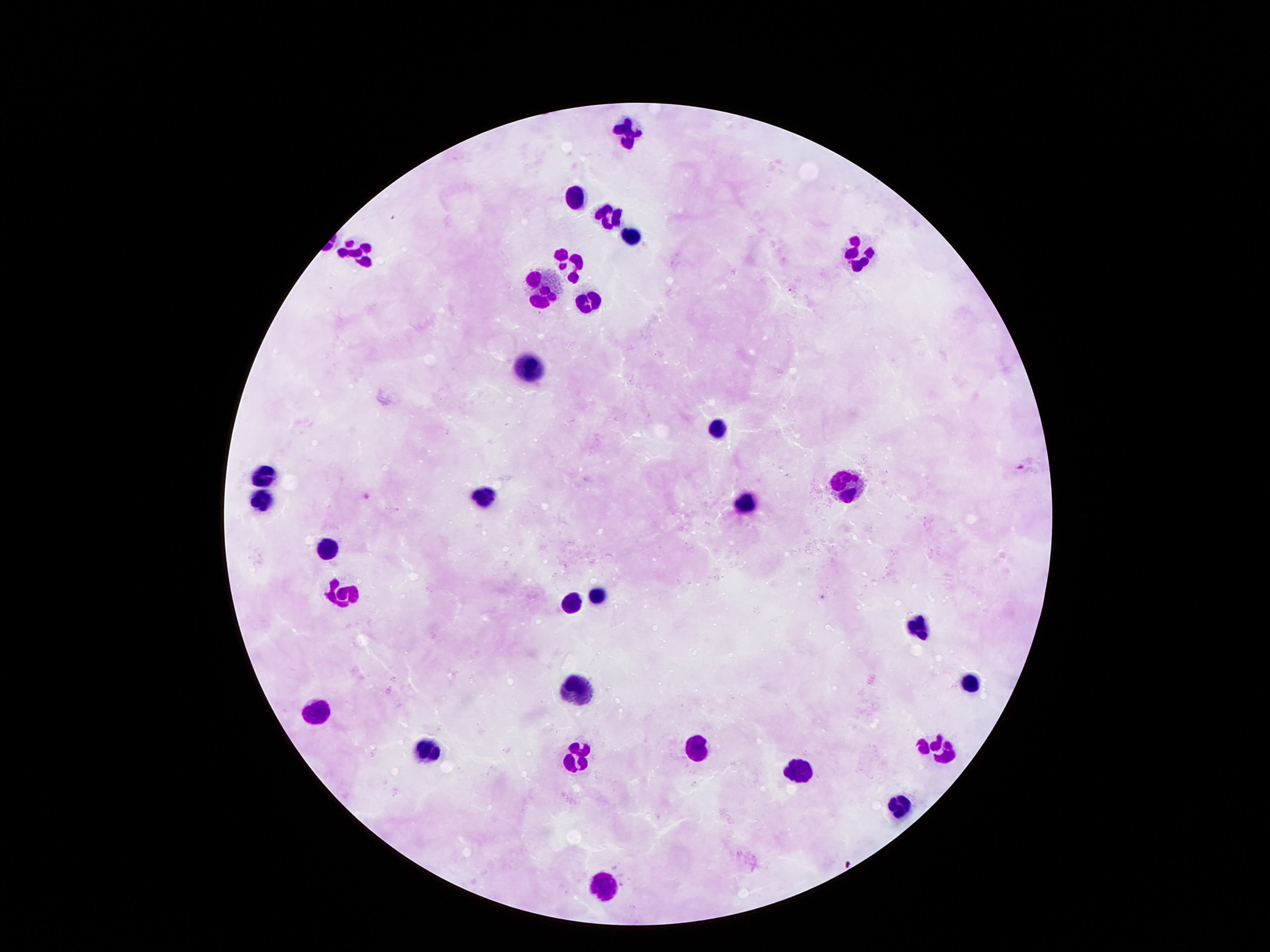

Approximate centers as (x, y) in pixels.
Summary:
  - Leukocyte locations: (630, 128), (575, 198), (606, 209), (634, 236), (861, 250), (357, 253), (572, 264), (545, 290), (589, 295), (530, 369), (719, 428), (267, 474), (849, 482), (484, 496), (263, 497), (746, 498), (329, 551), (598, 593), (342, 596), (568, 601), (913, 627), (973, 682), (576, 684), (315, 715), (696, 744), (937, 746), (429, 752), (578, 754), (802, 768), (899, 805), (604, 883)
  - Field of view: single
  - Magnification: 100x
  - Capture: smartphone camera through the microscope eyepiece
  - Preparation: thick blood film
  - Stain: Giemsa
  - Image size: 1270×952 pixels
  - Patient malaria status: not infected